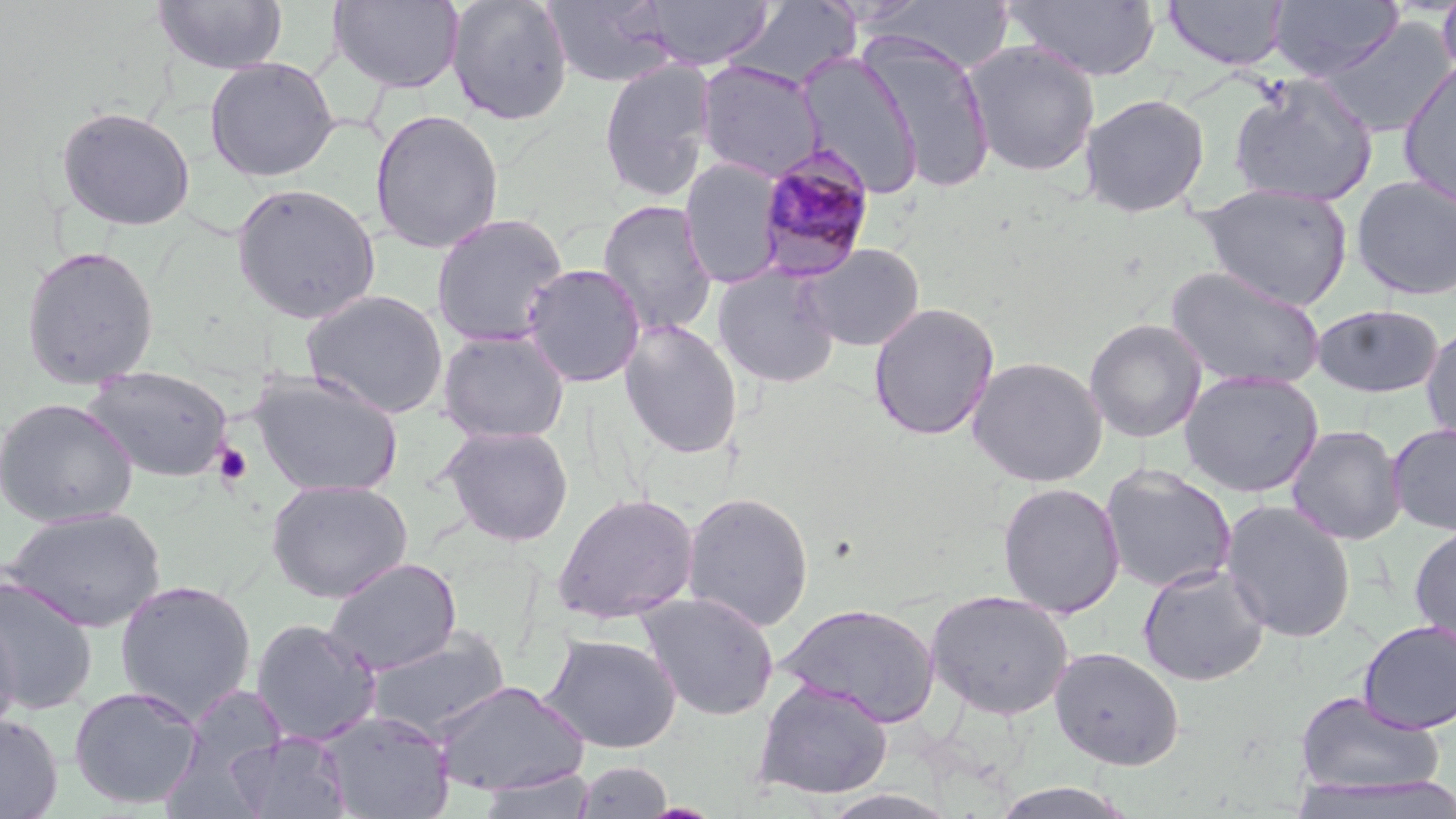

Summary:
  - Coordinate format: approximate bounding boxes as [x1, y1, x2, y2] in pixels
  - Platelet locations: [213, 443, 253, 486]
  - Uninfected red blood cell locations: [329, 0, 465, 93], [446, 0, 573, 126], [543, 0, 677, 89], [641, 0, 774, 70], [1004, 0, 1161, 82], [1161, 0, 1290, 71], [1268, 0, 1404, 80], [1436, 0, 1456, 83], [153, 1, 288, 75], [727, 1, 861, 91], [865, 1, 1019, 76], [1319, 17, 1454, 139], [860, 31, 997, 195], [963, 40, 1101, 178], [796, 51, 924, 200], [204, 56, 340, 182], [597, 57, 717, 203], [1397, 58, 1456, 211], [694, 60, 825, 183], [1228, 74, 1378, 207], [1079, 93, 1211, 218], [55, 105, 197, 232], [369, 108, 505, 255], [678, 157, 787, 288], [1351, 175, 1456, 302], [231, 182, 382, 324], [1195, 184, 1354, 310], [596, 199, 718, 337], [430, 212, 569, 347], [798, 243, 926, 351], [19, 244, 161, 390], [520, 263, 646, 388], [712, 265, 841, 389], [1165, 265, 1326, 392], [301, 289, 450, 419], [867, 301, 1000, 441], [1311, 304, 1446, 398], [618, 318, 744, 459], [1084, 318, 1207, 443], [1421, 325, 1456, 445], [436, 329, 570, 444], [967, 355, 1108, 487], [83, 365, 235, 483], [1179, 369, 1324, 498], [248, 370, 403, 498], [0, 396, 138, 528], [1387, 422, 1456, 536], [439, 424, 575, 546], [1285, 424, 1407, 545], [1098, 464, 1239, 594], [265, 479, 413, 602], [996, 481, 1125, 619], [681, 491, 815, 632], [552, 492, 700, 625], [1220, 499, 1357, 642], [2, 506, 167, 633], [1409, 524, 1456, 649], [323, 557, 462, 676], [1137, 562, 1271, 687], [0, 573, 99, 716], [113, 579, 258, 723], [925, 589, 1075, 720], [635, 590, 781, 722], [777, 602, 942, 727], [0, 609, 21, 742], [249, 618, 381, 746], [1357, 619, 1456, 734], [365, 627, 512, 741], [541, 633, 682, 754], [1048, 646, 1185, 771], [752, 679, 893, 801], [432, 680, 588, 796], [68, 685, 203, 810], [167, 686, 291, 807], [1293, 691, 1447, 798], [318, 709, 454, 818], [0, 712, 64, 819], [226, 729, 352, 819], [574, 761, 674, 818], [475, 768, 595, 818], [1293, 772, 1454, 819], [988, 781, 1141, 818]
  - Plasmodium malariae-infected red blood cell locations: [755, 144, 877, 280]
  - Slide-level diagnosis: Plasmodium malariae
  - Image size: 1456×819 pixels
  - Preparation: thin blood smear
  - Magnification: 1000x
  - Modality: optical microscopy
  - Stain: May-Grünwald-Giemsa
  - Field of view: single